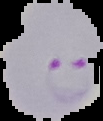
preparation = thin blood film
image size = 103×121 pixels
malaria status = parasitized
image type = segmented cell region on a black background